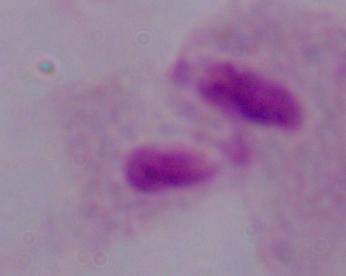
Captured at 1000x magnification. A trichomonad is shown. Micrograph.